Assess this cell for malaria.
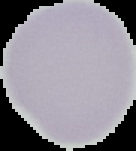

It is uninfected.

image_size: 136×151 pixels
preparation: thin blood film
image_type: cell region segmented out of the field of view; surrounding area masked to black